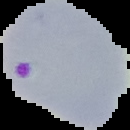

Segmented cell region on a black background. Image is 130×130 pixels. Malaria status: parasitized. From a thin blood smear.